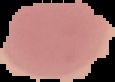
Summary:
  - Preparation: thin blood smear
  - Image size: 115×82 pixels
  - Result: no malaria parasites seen
  - Image type: segmented cell region on a black background